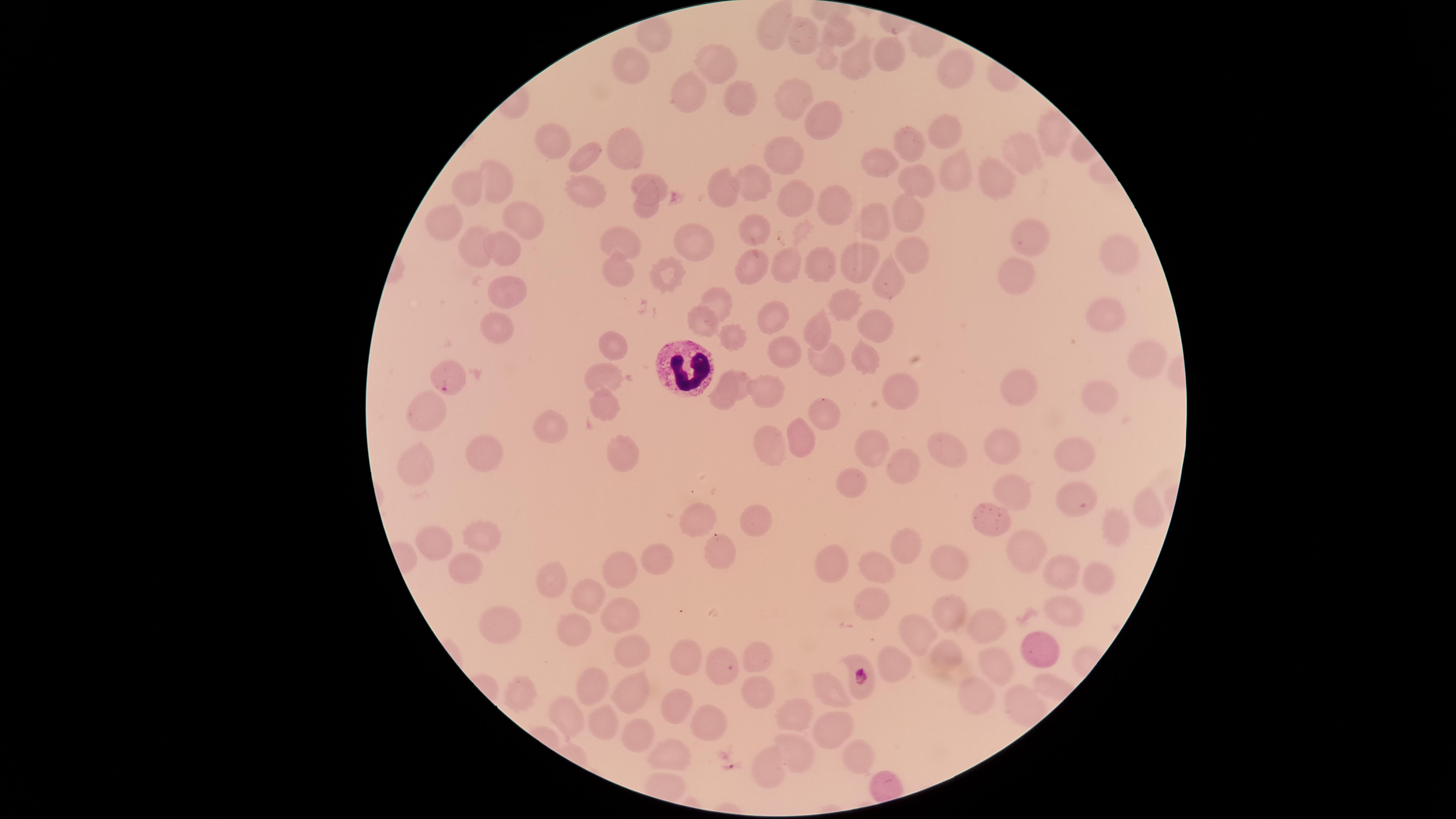
Approximate marker points as (x, y) in pixels. WBCs: (684, 368). Parasitized RBCs: (446, 379), (859, 672). Uninfected RBCs: (786, 21), (840, 32), (800, 35), (891, 56), (859, 61), (711, 64), (629, 69), (960, 70), (687, 89), (737, 99), (797, 99), (824, 118), (951, 133), (1044, 133), (552, 141), (909, 144), (621, 151), (1024, 152), (788, 154), (585, 158), (885, 166), (955, 170), (1002, 173), (501, 177), (649, 181), (751, 182), (473, 183), (919, 183), (720, 187), (586, 188), (796, 192), (834, 206), (643, 210), (906, 211), (445, 219), (515, 224), (757, 228), (876, 228), (1027, 236), (698, 241), (478, 244), (620, 246), (911, 246), (505, 249), (1119, 254), (853, 260), (750, 266), (824, 266), (788, 269), (619, 270), (669, 272), (891, 277), (1008, 277), (505, 294), (840, 304), (717, 305), (1104, 310), (774, 316), (882, 319), (498, 321), (703, 323), (820, 326), (730, 337), (616, 347), (785, 356), (866, 360), (823, 361), (1139, 365), (604, 373), (1013, 385), (732, 386), (898, 386), (768, 392), (1098, 395), (428, 404), (602, 409), (824, 411), (552, 423), (798, 434), (764, 440), (950, 447), (1004, 447), (873, 450), (488, 456), (626, 456), (1079, 456), (420, 464), (899, 465), (852, 482), (1010, 495), (1068, 498), (703, 519), (756, 519), (1147, 519), (986, 521), (1114, 527), (478, 534), (428, 542), (903, 542), (711, 550), (1024, 551), (657, 559), (831, 559), (948, 560), (875, 565), (464, 570), (619, 571), (1065, 572), (550, 581), (1096, 584), (589, 595), (872, 605), (1057, 613), (618, 614), (948, 618), (985, 619), (507, 627), (575, 631), (917, 632), (1035, 646), (948, 652), (628, 653), (689, 654), (757, 659), (999, 665), (885, 666), (722, 668), (593, 688), (834, 690), (523, 691), (629, 692), (758, 695), (978, 695), (1020, 704), (679, 705), (794, 714), (571, 718), (607, 723), (708, 723), (835, 729), (645, 731), (666, 751), (798, 754), (859, 757), (763, 769). Single field of view. Species: Plasmodium falciparum. Giemsa stain. Image is 1456×819 pixels. Thin smear of blood. Smartphone photograph through the microscope eyepiece. Presence: malaria parasites detected. Circular visible region.